Locate every malaria parasite.
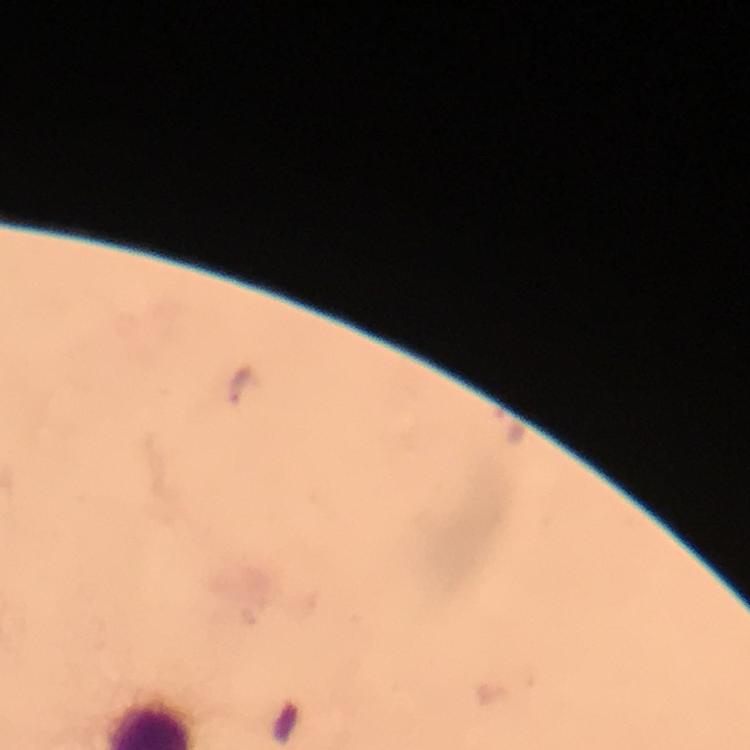
Approximate centers as {x, y} in pixels.
Malaria parasites: {241, 387}.

cropped from = a single field of view
immersion oil = used
magnification = 100x
image size = 750×750 pixels
context = from a diagnostic examination for malaria
preparation = thick blood smear
capture = smartphone mounted on the microscope
stain = Giemsa